Assess this cell for malaria.
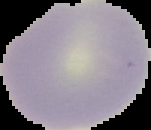
Uninfected.

Summary:
  - Image size: 151×130 pixels
  - Image type: segmented cell region with the area outside set to black
  - Preparation: thin blood smear